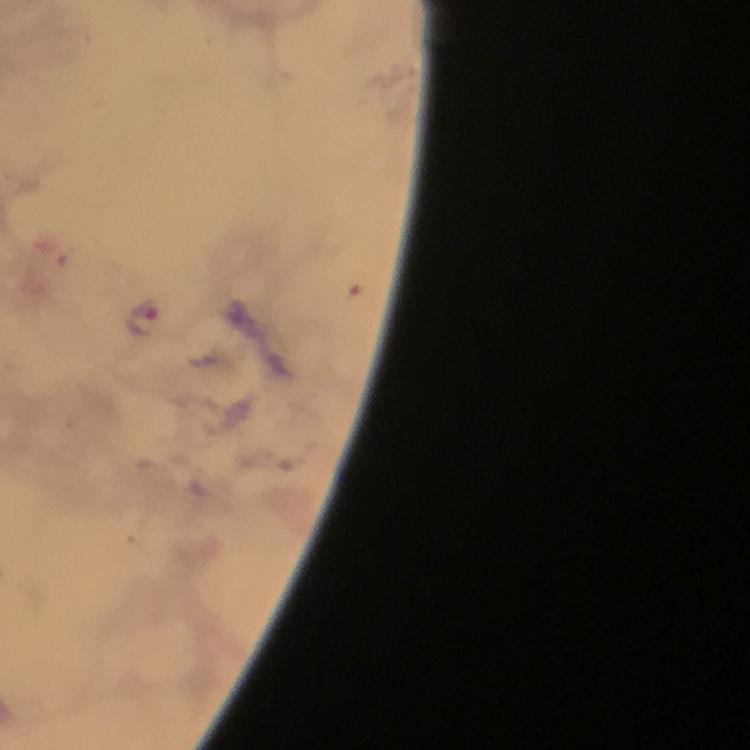

Approximate centers as {x, y} in pixels.
Summary:
  - Malaria parasite locations: {143, 318}
  - Immersion oil: applied
  - Cropped from: a single field of view
  - Magnification: 100x
  - Stain: Giemsa
  - Preparation: thick smear
  - Image size: 750×750 pixels
  - Context: from a diagnostic examination for malaria
  - Capture: smartphone camera through the microscope